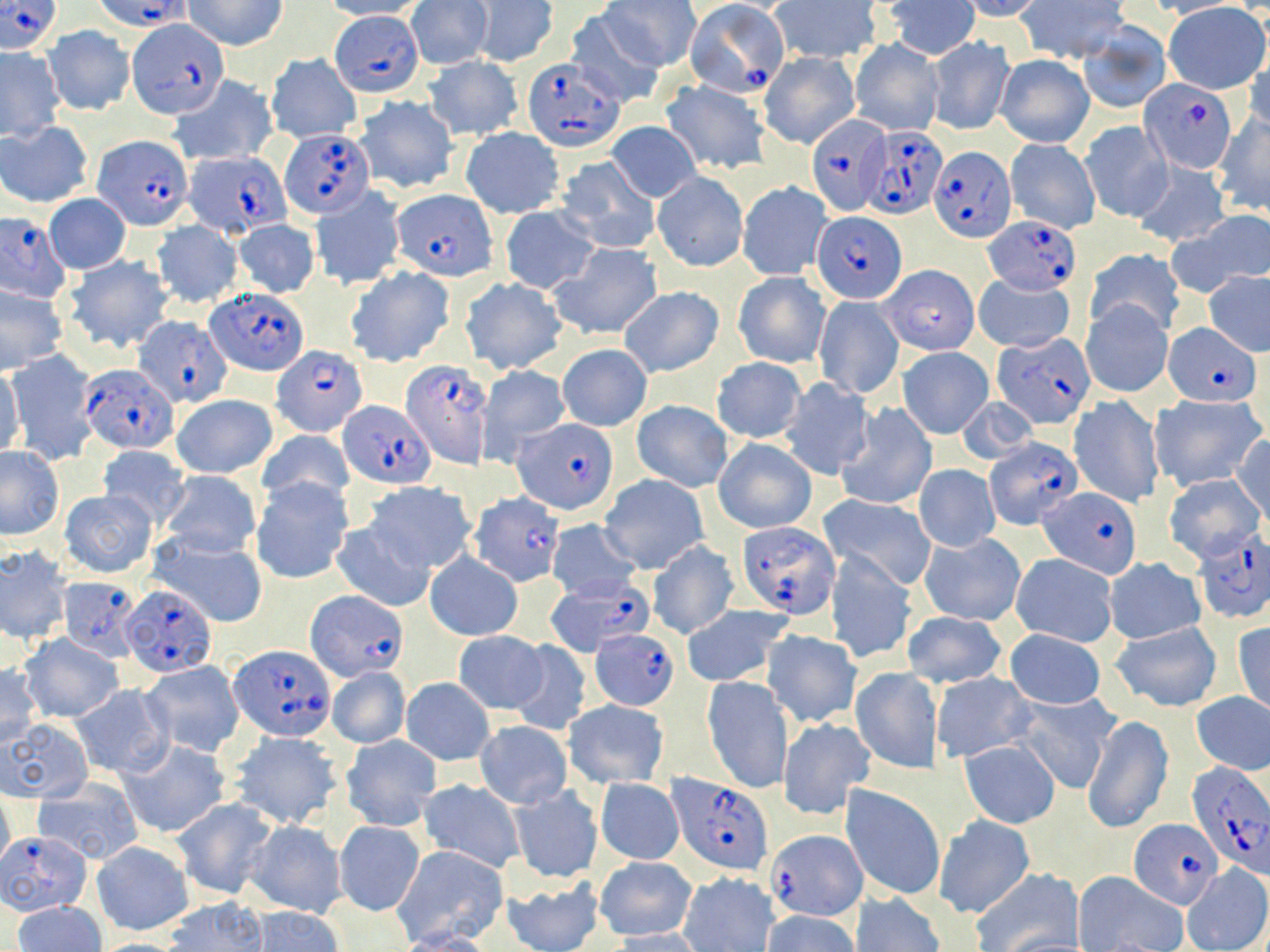
Approximate bounding boxes as named x1/y1/x2/y2 corners in pixels. Uninfected red blood cell locations: (x1=184, y1=0, x2=287, y2=51), (x1=319, y1=0, x2=428, y2=20), (x1=601, y1=0, x2=700, y2=71), (x1=882, y1=0, x2=980, y2=60), (x1=960, y1=0, x2=1048, y2=22), (x1=1018, y1=0, x2=1130, y2=64), (x1=1142, y1=0, x2=1246, y2=19), (x1=406, y1=1, x2=491, y2=70), (x1=469, y1=1, x2=557, y2=68), (x1=769, y1=1, x2=885, y2=62), (x1=1163, y1=3, x2=1269, y2=93), (x1=561, y1=9, x2=666, y2=107), (x1=1078, y1=21, x2=1171, y2=113), (x1=43, y1=26, x2=134, y2=115), (x1=926, y1=36, x2=1014, y2=134), (x1=4, y1=38, x2=115, y2=128), (x1=850, y1=39, x2=943, y2=136), (x1=0, y1=48, x2=65, y2=138), (x1=1242, y1=50, x2=1270, y2=136), (x1=760, y1=52, x2=860, y2=148), (x1=266, y1=54, x2=361, y2=143), (x1=994, y1=54, x2=1094, y2=148), (x1=423, y1=56, x2=524, y2=141), (x1=167, y1=75, x2=277, y2=167), (x1=661, y1=79, x2=773, y2=175), (x1=354, y1=95, x2=459, y2=194), (x1=1212, y1=114, x2=1270, y2=215), (x1=1081, y1=119, x2=1171, y2=223), (x1=0, y1=121, x2=92, y2=206), (x1=606, y1=121, x2=700, y2=202), (x1=460, y1=127, x2=565, y2=218), (x1=1006, y1=138, x2=1100, y2=234), (x1=556, y1=156, x2=660, y2=255), (x1=1132, y1=159, x2=1231, y2=247), (x1=653, y1=171, x2=748, y2=271), (x1=737, y1=181, x2=832, y2=280), (x1=311, y1=185, x2=405, y2=289), (x1=44, y1=194, x2=131, y2=273), (x1=500, y1=206, x2=598, y2=295), (x1=1182, y1=211, x2=1270, y2=291), (x1=232, y1=218, x2=320, y2=298), (x1=150, y1=221, x2=243, y2=308), (x1=549, y1=242, x2=663, y2=340), (x1=1085, y1=248, x2=1184, y2=335), (x1=64, y1=255, x2=174, y2=354), (x1=346, y1=266, x2=456, y2=366), (x1=1203, y1=270, x2=1270, y2=356), (x1=733, y1=272, x2=831, y2=368), (x1=974, y1=272, x2=1074, y2=354), (x1=459, y1=276, x2=568, y2=375), (x1=0, y1=285, x2=67, y2=372), (x1=619, y1=287, x2=724, y2=377), (x1=814, y1=294, x2=903, y2=399), (x1=1081, y1=298, x2=1173, y2=397), (x1=558, y1=344, x2=652, y2=431), (x1=897, y1=347, x2=994, y2=438), (x1=6, y1=352, x2=98, y2=464), (x1=711, y1=358, x2=806, y2=442), (x1=477, y1=364, x2=571, y2=465), (x1=0, y1=365, x2=25, y2=461), (x1=778, y1=377, x2=875, y2=478), (x1=1151, y1=393, x2=1265, y2=492), (x1=172, y1=394, x2=277, y2=480), (x1=1069, y1=395, x2=1163, y2=508), (x1=956, y1=396, x2=1038, y2=466), (x1=632, y1=400, x2=732, y2=491), (x1=836, y1=402, x2=937, y2=511), (x1=258, y1=427, x2=354, y2=510), (x1=1230, y1=433, x2=1270, y2=524), (x1=713, y1=436, x2=817, y2=534), (x1=96, y1=445, x2=190, y2=528), (x1=0, y1=448, x2=64, y2=539), (x1=915, y1=465, x2=999, y2=552), (x1=159, y1=469, x2=262, y2=558), (x1=1163, y1=472, x2=1267, y2=565), (x1=600, y1=476, x2=708, y2=573), (x1=250, y1=478, x2=353, y2=584), (x1=365, y1=482, x2=475, y2=573), (x1=61, y1=489, x2=157, y2=577), (x1=819, y1=494, x2=938, y2=588), (x1=545, y1=519, x2=641, y2=602), (x1=332, y1=521, x2=435, y2=611), (x1=149, y1=531, x2=270, y2=630), (x1=920, y1=533, x2=1026, y2=626), (x1=646, y1=541, x2=737, y2=639), (x1=0, y1=547, x2=72, y2=645), (x1=826, y1=549, x2=917, y2=664), (x1=424, y1=552, x2=523, y2=641), (x1=1011, y1=553, x2=1119, y2=646), (x1=1105, y1=558, x2=1205, y2=644), (x1=680, y1=604, x2=795, y2=688), (x1=902, y1=611, x2=1007, y2=689), (x1=1233, y1=621, x2=1270, y2=717), (x1=1111, y1=622, x2=1224, y2=711), (x1=1004, y1=628, x2=1107, y2=709), (x1=763, y1=629, x2=862, y2=727), (x1=452, y1=630, x2=548, y2=713), (x1=18, y1=635, x2=124, y2=722), (x1=507, y1=639, x2=592, y2=736), (x1=137, y1=660, x2=245, y2=757), (x1=0, y1=664, x2=40, y2=749), (x1=326, y1=666, x2=410, y2=748), (x1=851, y1=668, x2=942, y2=774), (x1=930, y1=673, x2=1035, y2=762), (x1=703, y1=676, x2=792, y2=793), (x1=402, y1=677, x2=494, y2=764), (x1=69, y1=685, x2=174, y2=778), (x1=1014, y1=691, x2=1120, y2=793), (x1=1191, y1=692, x2=1270, y2=775), (x1=564, y1=700, x2=669, y2=788), (x1=1082, y1=714, x2=1173, y2=835), (x1=779, y1=717, x2=875, y2=819), (x1=1, y1=718, x2=91, y2=801), (x1=475, y1=721, x2=572, y2=807), (x1=228, y1=732, x2=342, y2=830), (x1=341, y1=735, x2=440, y2=831), (x1=959, y1=739, x2=1061, y2=828), (x1=120, y1=740, x2=230, y2=838), (x1=597, y1=778, x2=683, y2=865), (x1=418, y1=779, x2=525, y2=872), (x1=33, y1=781, x2=143, y2=865), (x1=840, y1=785, x2=945, y2=901), (x1=509, y1=786, x2=602, y2=883), (x1=0, y1=791, x2=15, y2=874), (x1=173, y1=798, x2=277, y2=900), (x1=933, y1=815, x2=1036, y2=919), (x1=243, y1=820, x2=347, y2=917), (x1=333, y1=820, x2=425, y2=917), (x1=91, y1=840, x2=193, y2=934), (x1=392, y1=844, x2=507, y2=946), (x1=594, y1=857, x2=698, y2=940), (x1=1182, y1=864, x2=1270, y2=952), (x1=969, y1=868, x2=1081, y2=952), (x1=679, y1=871, x2=780, y2=951), (x1=1074, y1=871, x2=1189, y2=952), (x1=501, y1=875, x2=604, y2=952), (x1=850, y1=893, x2=945, y2=952), (x1=161, y1=896, x2=267, y2=951), (x1=12, y1=901, x2=106, y2=952), (x1=246, y1=906, x2=345, y2=952), (x1=761, y1=910, x2=860, y2=952), (x1=605, y1=929, x2=710, y2=952), (x1=388, y1=930, x2=498, y2=952). Plasmodium falciparum-infected red blood cell locations: (x1=99, y1=0, x2=191, y2=30), (x1=1, y1=1, x2=62, y2=54), (x1=684, y1=2, x2=791, y2=99), (x1=331, y1=12, x2=423, y2=94), (x1=128, y1=17, x2=225, y2=118), (x1=521, y1=58, x2=624, y2=150), (x1=1139, y1=79, x2=1239, y2=172), (x1=806, y1=114, x2=890, y2=215), (x1=862, y1=123, x2=948, y2=218), (x1=280, y1=128, x2=373, y2=216), (x1=95, y1=135, x2=192, y2=230), (x1=930, y1=147, x2=1015, y2=244), (x1=184, y1=149, x2=289, y2=236), (x1=394, y1=189, x2=497, y2=280), (x1=0, y1=212, x2=72, y2=303), (x1=812, y1=212, x2=908, y2=304), (x1=984, y1=214, x2=1081, y2=294), (x1=880, y1=264, x2=980, y2=355), (x1=206, y1=286, x2=309, y2=376), (x1=134, y1=316, x2=231, y2=406), (x1=1166, y1=323, x2=1262, y2=405), (x1=992, y1=332, x2=1095, y2=428), (x1=270, y1=345, x2=368, y2=436), (x1=401, y1=355, x2=497, y2=467), (x1=79, y1=365, x2=178, y2=453), (x1=341, y1=400, x2=435, y2=488), (x1=515, y1=420, x2=618, y2=514), (x1=985, y1=436, x2=1081, y2=526), (x1=1038, y1=486, x2=1139, y2=576), (x1=468, y1=492, x2=566, y2=587), (x1=735, y1=520, x2=839, y2=616), (x1=1192, y1=530, x2=1269, y2=622), (x1=59, y1=576, x2=143, y2=662), (x1=546, y1=577, x2=652, y2=656), (x1=121, y1=584, x2=216, y2=677), (x1=305, y1=591, x2=408, y2=680), (x1=590, y1=628, x2=680, y2=709), (x1=230, y1=646, x2=334, y2=741), (x1=1186, y1=763, x2=1270, y2=876), (x1=669, y1=773, x2=775, y2=874), (x1=1129, y1=817, x2=1222, y2=907), (x1=764, y1=830, x2=867, y2=924), (x1=2, y1=831, x2=96, y2=915). Slide-level diagnosis: Plasmodium falciparum. Single field of view. May-Grünwald-Giemsa-stained preparation. Optical microscopy. Image is 1270×952 pixels. Captured at 1000x magnification. Thin blood smear.